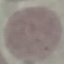

{
  "result": "no malaria parasites seen",
  "preparation": "thin smear",
  "image_type": "cell patch, automatically extracted from a larger field of view and resized to 64 × 64 pixels",
  "stain": "Giemsa",
  "capture": "smartphone through the microscope eyepiece"
}